Name the blood parasite species.
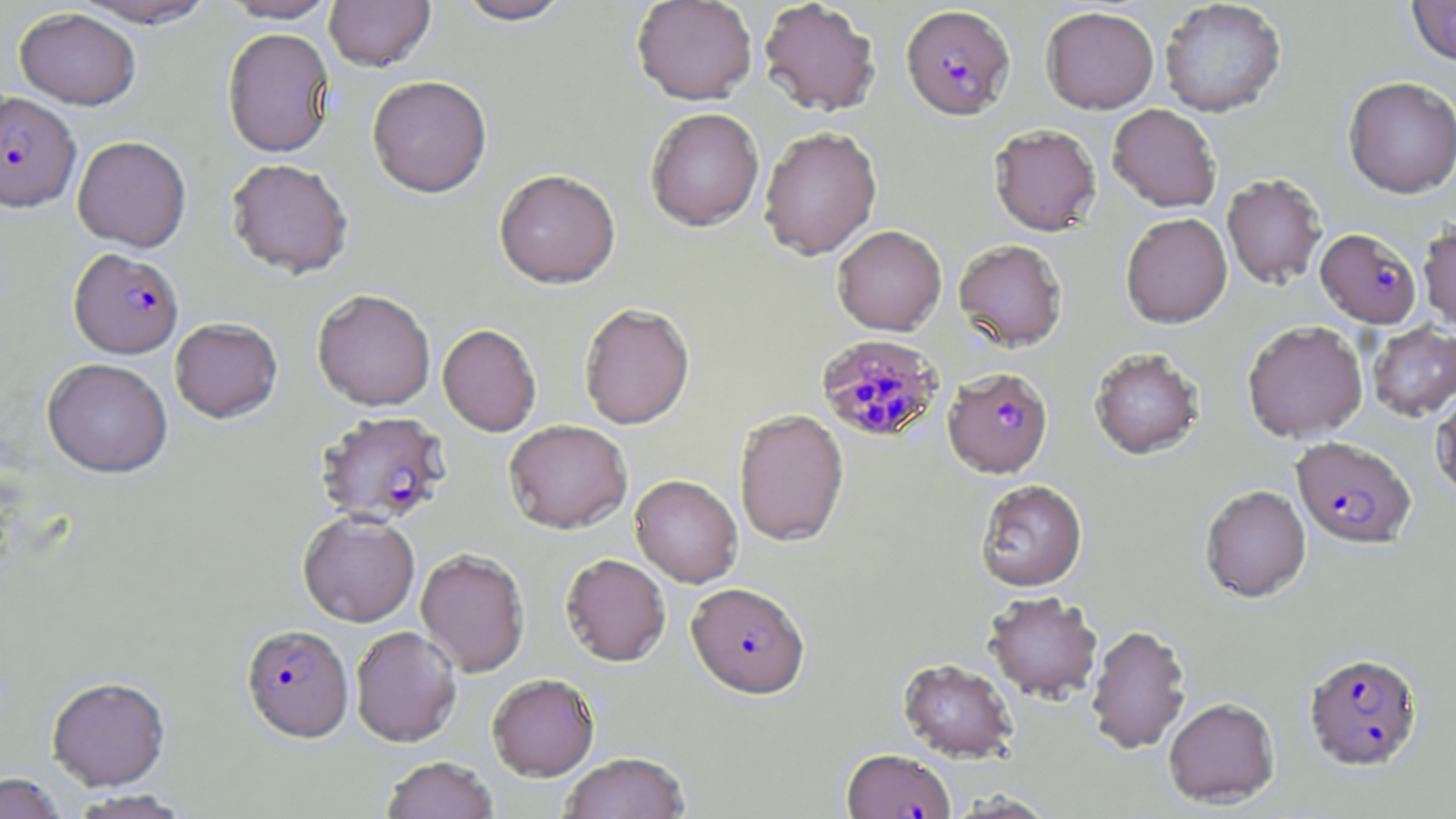

Plasmodium falciparum.

Summary:
  - Coordinate format: approximate bounding boxes as [x1, y1, x2, y2] in pixels
  - Plasmodium falciparum-infected red blood cell locations: [901, 4, 1015, 120], [1, 92, 80, 212], [1315, 228, 1422, 328], [69, 248, 184, 359], [816, 335, 944, 443], [943, 367, 1053, 478], [315, 410, 452, 525], [1291, 437, 1417, 550], [687, 582, 810, 699], [241, 624, 354, 742], [1303, 652, 1422, 771], [842, 749, 955, 819]
  - Uninfected red blood cell locations: [69, 0, 220, 28], [218, 0, 340, 23], [324, 0, 436, 71], [454, 0, 575, 25], [631, 0, 758, 105], [758, 0, 882, 116], [1159, 0, 1287, 117], [1407, 0, 1456, 66], [1041, 6, 1159, 113], [15, 8, 142, 110], [222, 27, 335, 158], [367, 75, 492, 197], [1343, 77, 1456, 198], [1107, 104, 1222, 212], [645, 107, 764, 231], [988, 123, 1102, 236], [759, 126, 882, 260], [72, 135, 192, 252], [226, 157, 354, 278], [494, 169, 621, 289], [1222, 173, 1327, 289], [1121, 213, 1232, 328], [1418, 219, 1456, 331], [832, 225, 947, 335], [953, 239, 1068, 351], [312, 289, 436, 411], [578, 302, 695, 430], [170, 317, 283, 423], [1242, 320, 1368, 442], [1367, 322, 1456, 422], [438, 323, 542, 436], [1089, 347, 1205, 460], [42, 358, 173, 478], [1430, 387, 1456, 500], [734, 408, 849, 547], [504, 419, 632, 534], [630, 474, 743, 588], [975, 479, 1088, 592], [1200, 485, 1311, 603], [298, 511, 420, 627], [415, 548, 530, 676], [560, 553, 670, 667], [983, 590, 1103, 703], [1086, 624, 1192, 755], [350, 626, 462, 747], [898, 658, 1018, 763], [487, 673, 599, 780], [46, 677, 171, 791], [1163, 698, 1280, 809], [558, 752, 690, 818], [381, 757, 498, 819], [0, 773, 66, 819], [69, 789, 192, 818], [946, 790, 1058, 818]
  - Image size: 1456×819 pixels
  - Modality: light microscopy
  - Magnification: 1000x
  - Field of view: one of a larger specimen
  - Stain: May-Grünwald-Giemsa
  - Preparation: thin blood film